Name the parasite shown.
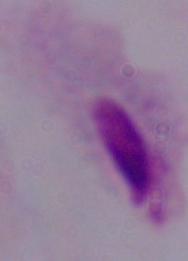

A trichomonad.

Micrograph. Captured at 1000x magnification.